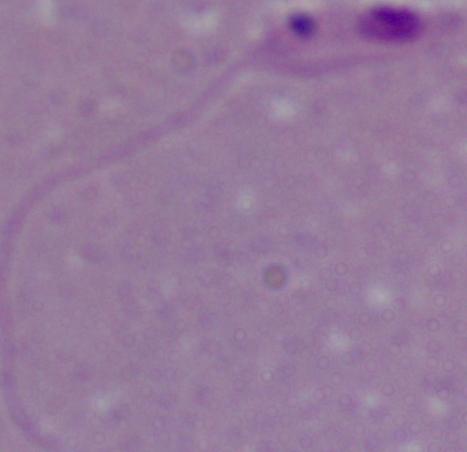

modality = micrograph
identification = Leishmania
magnification = 1000x